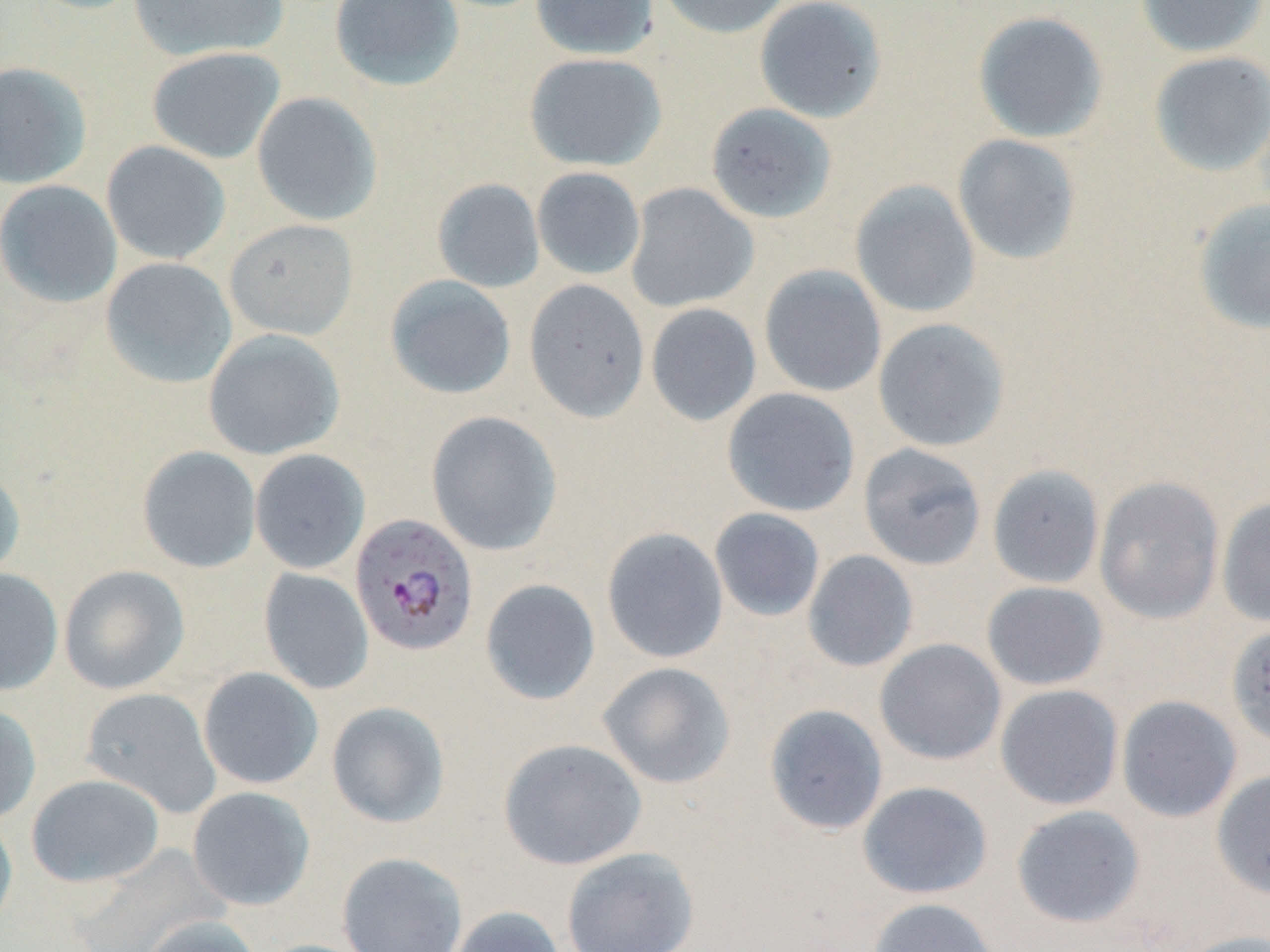

slide-level diagnosis = Plasmodium falciparum
uninfected red blood cell locations = approximate bounding boxes as named x1/y1/x2/y2 corners in pixels: (x1=128, y1=0, x2=289, y2=62), (x1=329, y1=0, x2=464, y2=91), (x1=530, y1=0, x2=659, y2=60), (x1=655, y1=0, x2=792, y2=39), (x1=754, y1=0, x2=888, y2=123), (x1=1136, y1=0, x2=1268, y2=58), (x1=973, y1=10, x2=1109, y2=144), (x1=146, y1=47, x2=286, y2=164), (x1=1149, y1=51, x2=1270, y2=177), (x1=524, y1=53, x2=667, y2=171), (x1=0, y1=61, x2=92, y2=189), (x1=252, y1=91, x2=383, y2=226), (x1=705, y1=103, x2=837, y2=224), (x1=952, y1=134, x2=1082, y2=265), (x1=101, y1=140, x2=231, y2=265), (x1=532, y1=167, x2=645, y2=280), (x1=432, y1=178, x2=545, y2=293), (x1=0, y1=179, x2=122, y2=308), (x1=850, y1=180, x2=981, y2=318), (x1=625, y1=183, x2=759, y2=313), (x1=1192, y1=198, x2=1270, y2=335), (x1=224, y1=219, x2=358, y2=340), (x1=100, y1=257, x2=237, y2=389), (x1=759, y1=265, x2=887, y2=397), (x1=384, y1=275, x2=517, y2=400), (x1=524, y1=279, x2=650, y2=422), (x1=646, y1=303, x2=762, y2=426), (x1=873, y1=318, x2=1011, y2=452), (x1=203, y1=328, x2=345, y2=459), (x1=722, y1=387, x2=860, y2=516), (x1=426, y1=410, x2=562, y2=556), (x1=858, y1=443, x2=987, y2=571), (x1=137, y1=446, x2=261, y2=573), (x1=249, y1=449, x2=370, y2=574), (x1=986, y1=464, x2=1105, y2=590), (x1=0, y1=467, x2=26, y2=583), (x1=1094, y1=476, x2=1225, y2=625), (x1=1216, y1=496, x2=1270, y2=628), (x1=709, y1=508, x2=825, y2=622), (x1=601, y1=527, x2=729, y2=664), (x1=802, y1=550, x2=919, y2=672), (x1=58, y1=565, x2=190, y2=694), (x1=259, y1=567, x2=374, y2=695), (x1=0, y1=568, x2=64, y2=695), (x1=480, y1=578, x2=601, y2=705), (x1=981, y1=581, x2=1109, y2=691), (x1=1226, y1=623, x2=1270, y2=750), (x1=874, y1=638, x2=1007, y2=766), (x1=597, y1=661, x2=736, y2=789), (x1=197, y1=667, x2=324, y2=790), (x1=995, y1=684, x2=1124, y2=810), (x1=80, y1=687, x2=222, y2=818), (x1=1116, y1=695, x2=1243, y2=823), (x1=326, y1=701, x2=450, y2=828), (x1=0, y1=703, x2=41, y2=826), (x1=764, y1=704, x2=888, y2=836), (x1=498, y1=737, x2=648, y2=871), (x1=1211, y1=768, x2=1270, y2=899), (x1=26, y1=774, x2=165, y2=888), (x1=857, y1=781, x2=993, y2=900), (x1=187, y1=786, x2=315, y2=910), (x1=1010, y1=805, x2=1146, y2=928), (x1=0, y1=813, x2=18, y2=934), (x1=560, y1=847, x2=700, y2=952), (x1=337, y1=852, x2=468, y2=952), (x1=867, y1=897, x2=1002, y2=952), (x1=446, y1=905, x2=566, y2=952), (x1=139, y1=915, x2=263, y2=952), (x1=1174, y1=930, x2=1270, y2=952)
stain = May-Grünwald-Giemsa
image size = 1270×952 pixels
field of view = single
preparation = thin blood smear
modality = light microscopy
Plasmodium falciparum-infected red blood cell locations = approximate bounding boxes as named x1/y1/x2/y2 corners in pixels: (x1=350, y1=513, x2=478, y2=656)
magnification = 1000x